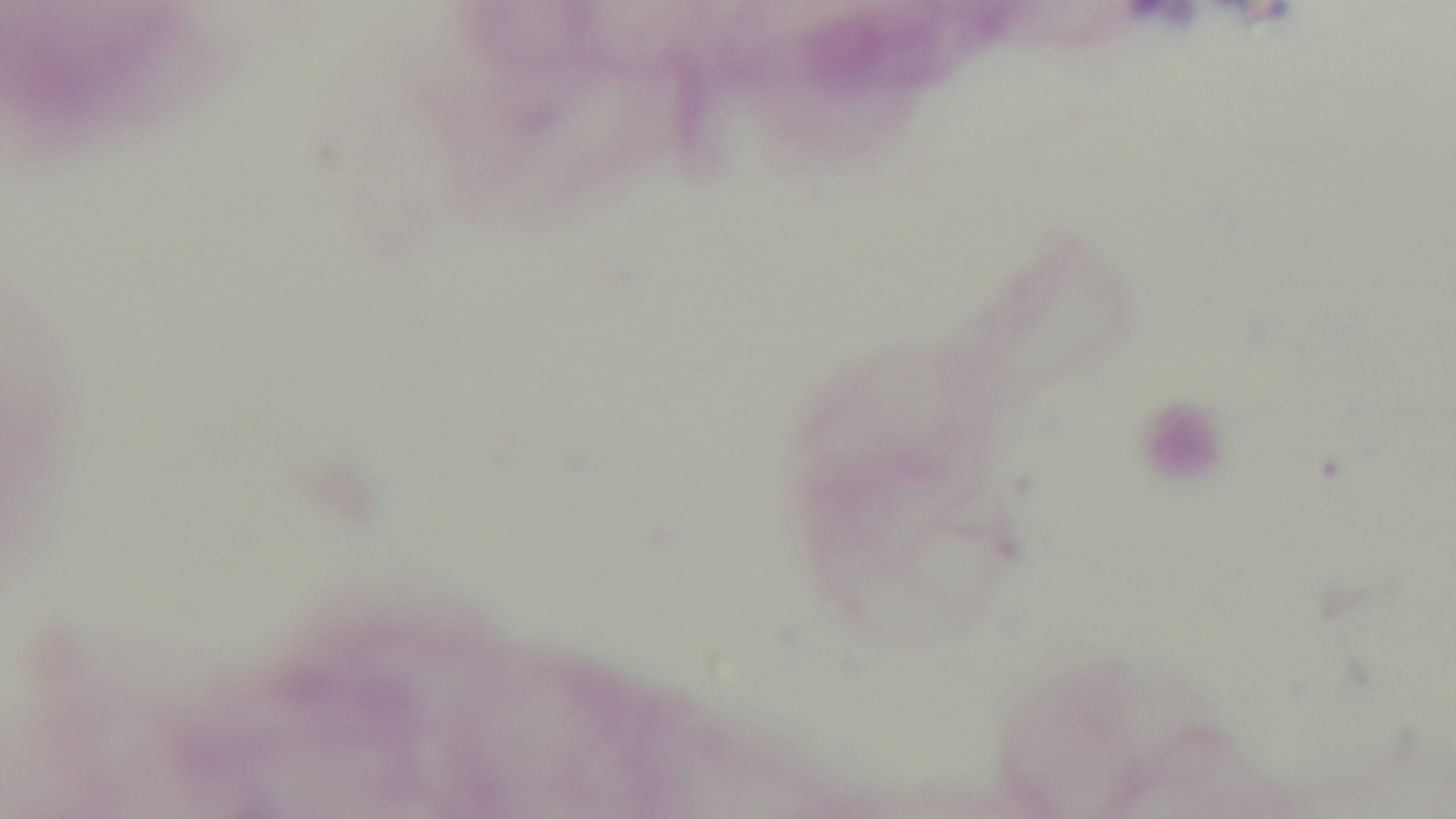
Mounted 4K digital camera. Photomicrograph. Oil-immersion objective, 100x. Giemsa-stained. Preparation: thick. One field from the slide. Malaria status: uninfected.